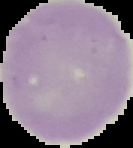 From a thin blood film. Image is 133×148 pixels. Segmented cell region on a black background. Malaria status: uninfected.